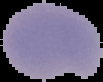

Image is 103×82 pixels. Segmented cell region on a black background. Result: no malaria parasites detected. From a thin blood smear.